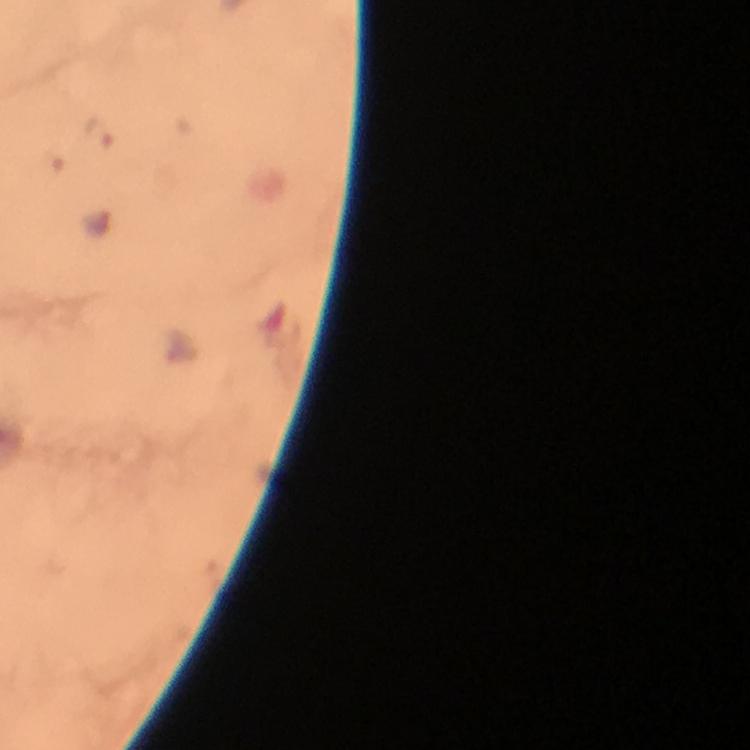
{
  "capture": "smartphone mounted on the microscope",
  "image_size": "750×750 pixels",
  "immersion_oil": "applied",
  "plasmodium_parasite_locations": "approximate object centers, in pixels from the top-left corner: (x=99, y=132)",
  "magnification": "100x",
  "cropped_from": "a single field of view",
  "stain": "Giemsa",
  "context": "from a malaria diagnostic workup",
  "preparation": "thick blood smear"
}